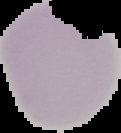
Summary:
  - Image type: segmented cell region on a black background
  - Image size: 121×133 pixels
  - Preparation: thin blood film
  - Result: no malaria parasites seen